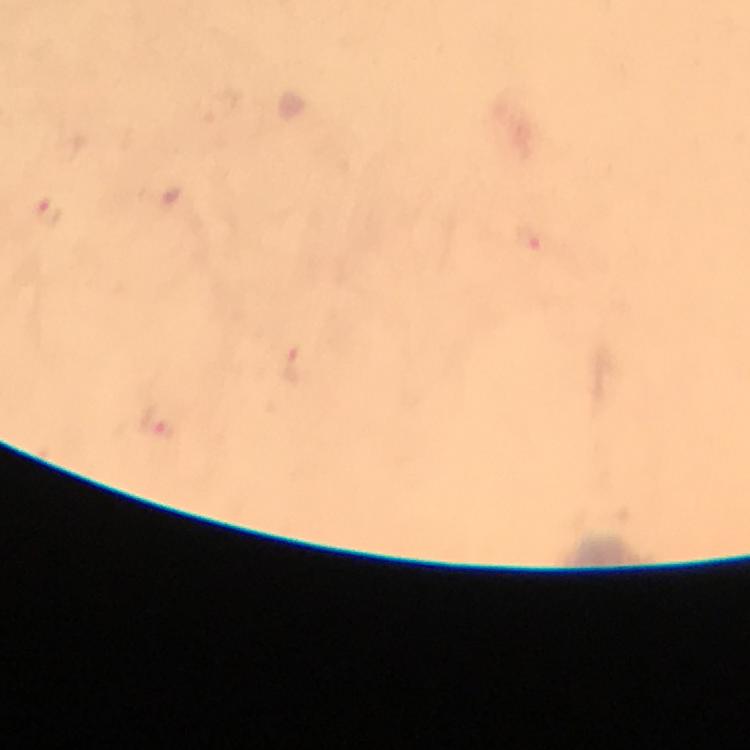

Approximate centers as (x, y) in pixels.
Summary:
  - Malaria parasite locations: (49, 212)
  - Immersion oil: used
  - Context: from a diagnostic examination for malaria
  - Magnification: 100x
  - Image size: 750×750 pixels
  - Stain: Giemsa
  - Preparation: thick smear
  - Cropped from: a single field of view
  - Capture: smartphone camera through the microscope